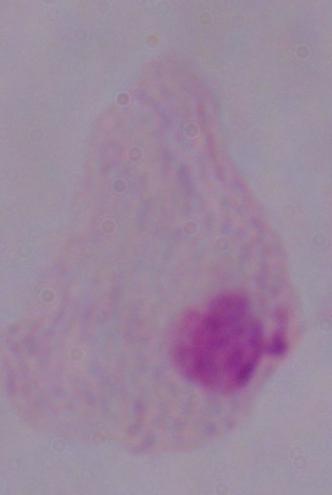

Summary:
  - Magnification: 1000x
  - Modality: photomicrograph
  - Identification: trichomonad